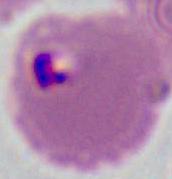
Summary:
  - Modality: photomicrograph
  - Identification: Plasmodium
  - Magnification: 400x or 1000x